Locate every blood parasite and identify its species.
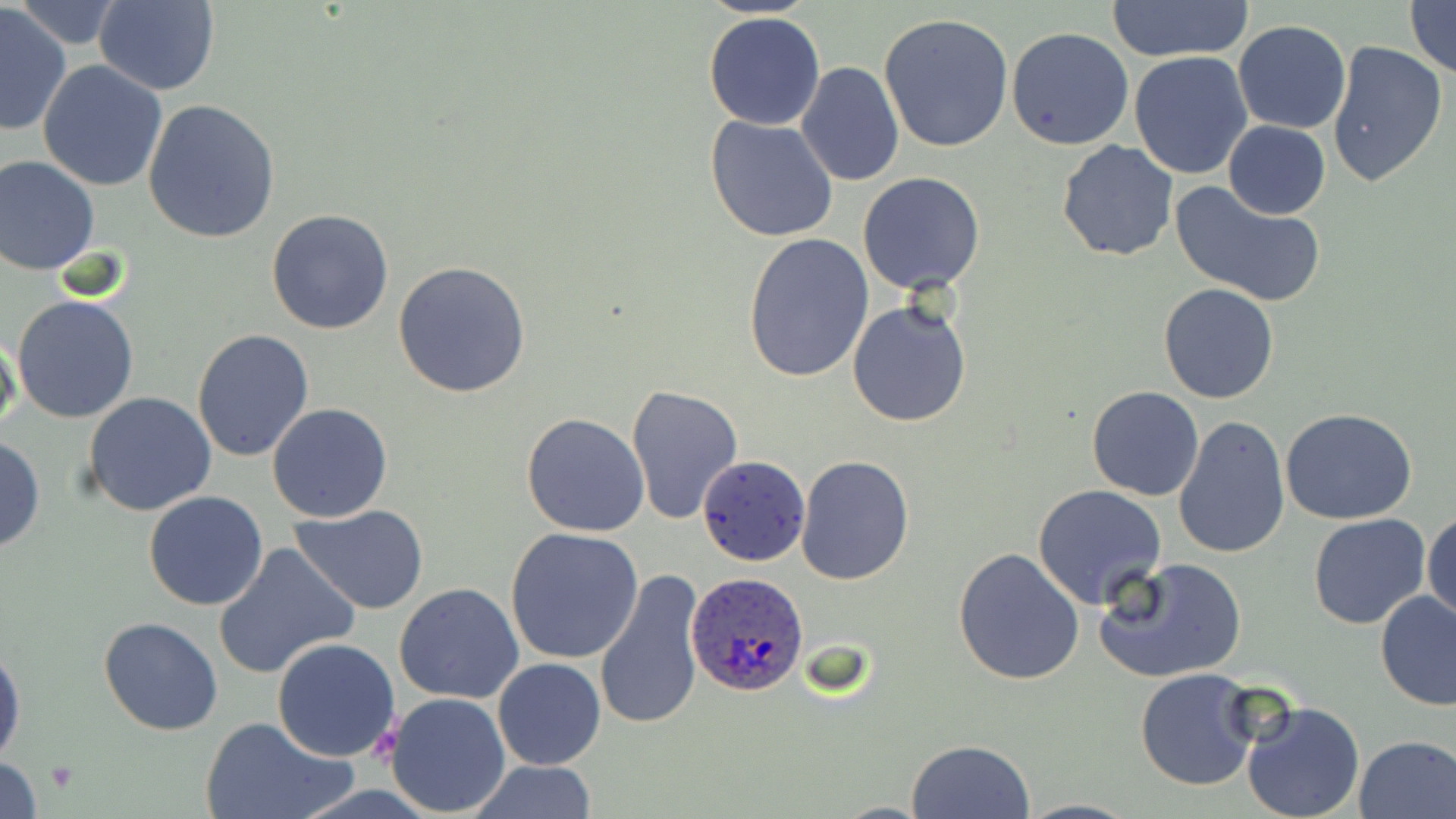

Approximate bounding boxes as (x1,y1)-(x2,y2) corner pairs in pixels.
Plasmodium ovale-infected red blood cells (subset): (687,574)-(807,698).
No Plasmodium falciparum, Plasmodium malariae, Plasmodium vivax, Babesia divergens, or Trypanosoma brucei observed.

Uninfected red blood cell locations (subset): (1111,0)-(1251,62), (1404,0)-(1455,79), (92,2)-(220,94), (0,3)-(74,138), (21,3)-(119,49), (702,10)-(827,130), (879,13)-(1014,151), (1232,20)-(1351,134), (1006,27)-(1135,150), (1327,38)-(1449,188), (1129,51)-(1253,179), (37,61)-(168,191), (795,61)-(905,185), (142,98)-(281,243), (704,116)-(839,243), (1224,120)-(1330,218), (1056,139)-(1178,262), (0,153)-(101,275), (857,172)-(987,295), (1169,180)-(1324,306), (266,208)-(396,335), (744,232)-(875,383), (392,261)-(532,399), (1158,282)-(1282,403), (12,295)-(140,424), (846,298)-(972,429), (191,328)-(315,465), (0,330)-(22,444), (625,384)-(745,524), (1086,387)-(1203,500), (83,392)-(217,517), (267,402)-(393,523), (1280,407)-(1417,524), (521,412)-(651,537), (1172,415)-(1290,561), (0,435)-(45,554), (795,454)-(915,585), (1031,483)-(1168,610), (143,491)-(268,611), (289,505)-(430,614), (1423,508)-(1456,628), (1308,514)-(1431,630), (504,528)-(645,665), (213,543)-(357,681), (952,547)-(1086,686), (1094,555)-(1248,683), (593,566)-(709,730), (1115,568)-(1254,783), (394,582)-(524,705), (1376,591)-(1456,711), (97,616)-(222,736), (272,637)-(401,760), (0,638)-(24,769), (493,658)-(606,770), (1134,669)-(1260,793), (384,692)-(512,814), (1239,699)-(1366,819), (202,715)-(352,819), (1353,735)-(1456,818), (906,738)-(1035,819), (0,755)-(43,817), (463,761)-(600,817). Platelet locations: (372,724)-(402,761), (47,762)-(76,792). Slide-level diagnosis: Plasmodium ovale. Thin blood film. Image is 1456×819 pixels. Captured at 1000x magnification. Light microscopy. Single field of view. May-Grünwald-Giemsa-stained preparation.